Assess this cell for malaria.
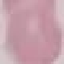

It is uninfected.

Summary:
  - Preparation: thin blood film
  - Image type: automatically extracted cell patch, resized to 64 × 64 pixels
  - Stain: Giemsa
  - Capture: smartphone through the microscope eyepiece